Assess this cell for malaria.
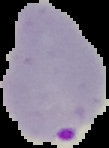

Parasitized.

Image is 109×148 pixels. From a thin blood smear. Segmented cell region on a black background.